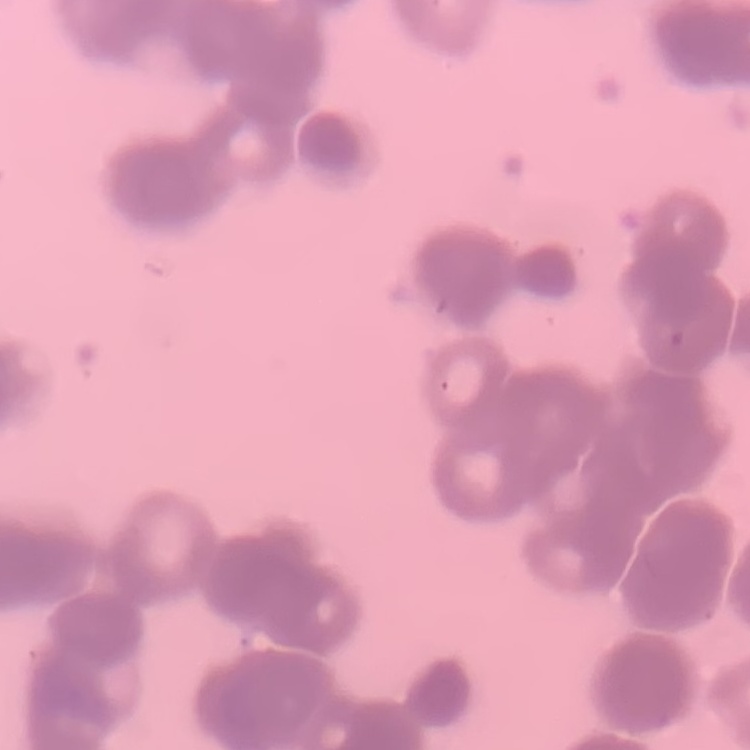

The erythrocytes show rouleaux formation. Thin peripheral smear. Field's or Giemsa stain. Square crop of a larger photomicrograph.